Point out each Plasmodium parasite.
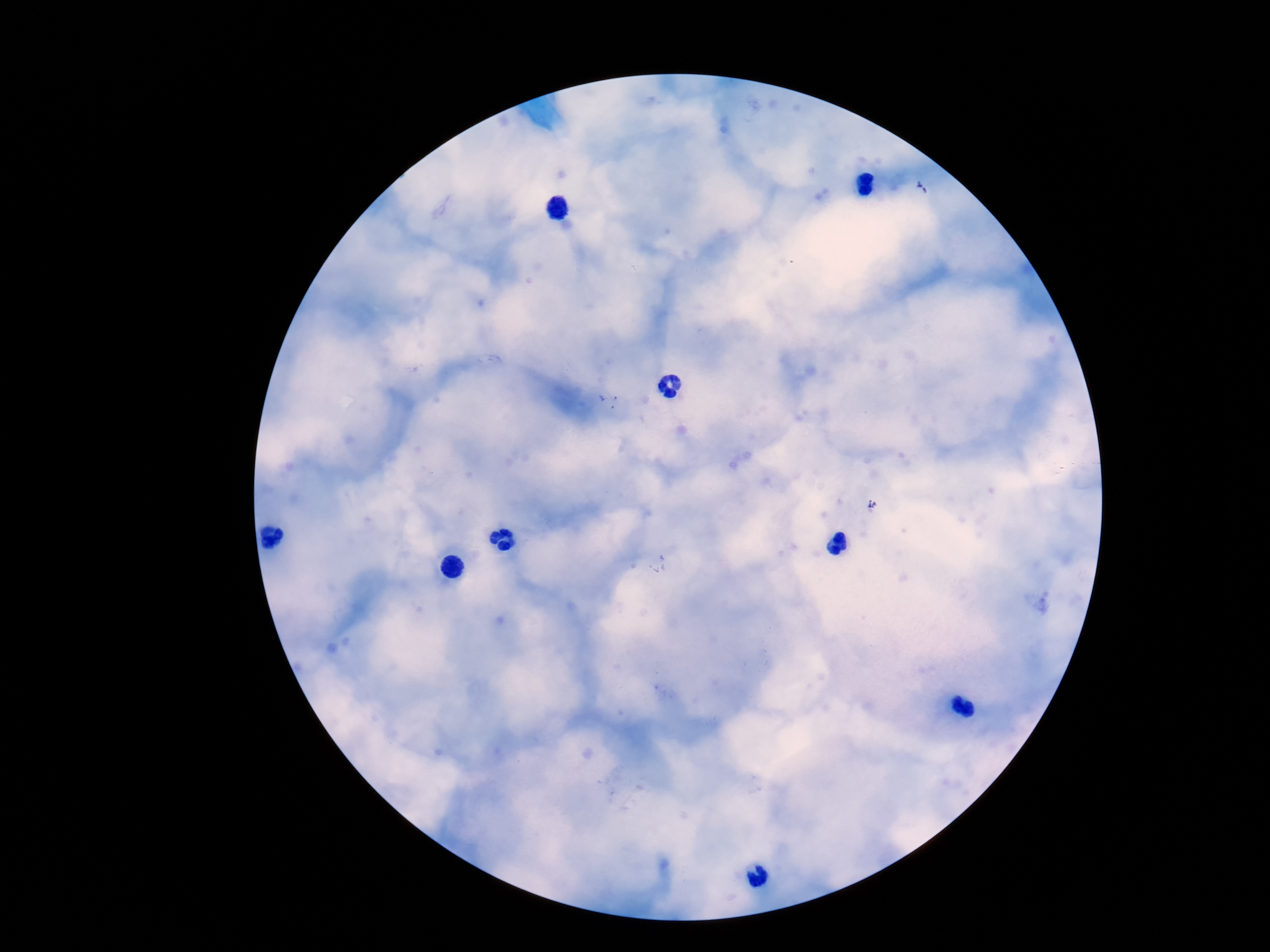
Approximate centers as [x, y] in pixels.
Plasmodium parasites: [609, 399].

Image is 1270×952 pixels. Photographed through the microscope eyepiece with a smartphone camera. Patient malaria status: infected. 100x magnification. One field from this slide. Giemsa-stained preparation. Thick peripheral-blood smear.